Report the malaria status of this cell.
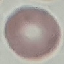
It is uninfected.

Acquired by smartphone through the microscope eyepiece. Automatically extracted cell patch, resized to 64 × 64 pixels. Thin blood smear. Giemsa-stained preparation.